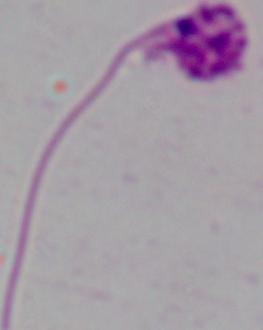

{
  "magnification": "1000x",
  "identification": "Leishmania",
  "modality": "micrograph"
}